Describe the morphology of the red blood cells.
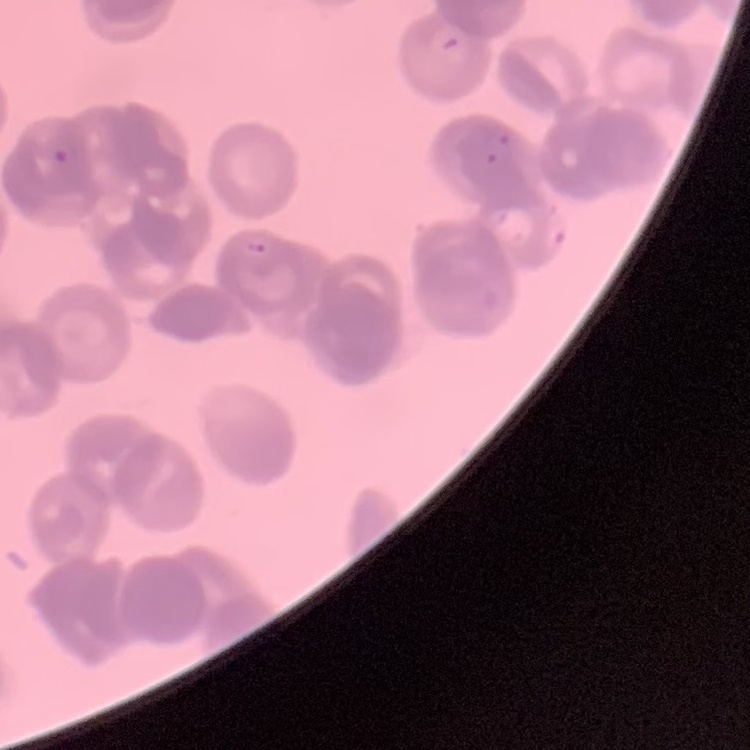

Rouleaux formation.

Thin peripheral smear. Stained with either Field's or Giemsa. One tile cut from a larger photomicrograph.